Name the parasite shown.
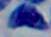
This is Toxoplasma gondii.

Captured at 1000x magnification. Micrograph.